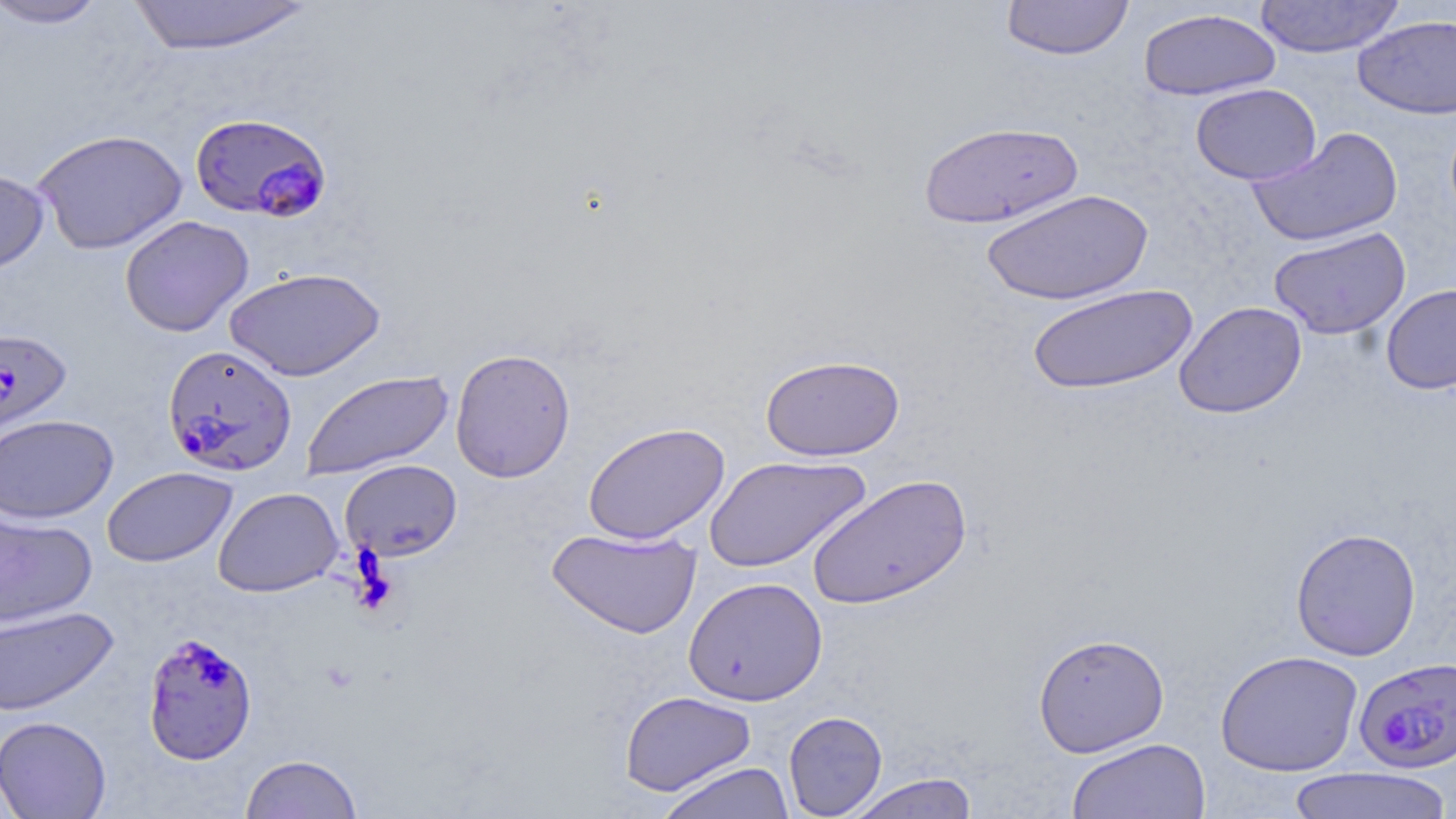

Approximate bounding boxes as (x1,y1)-(x2,y2) corner pairs in pixels. Plasmodium falciparum-infected red blood cell locations: (189,112)-(332,222), (0,328)-(72,443), (163,344)-(297,477), (142,630)-(258,765), (1353,657)-(1456,775). Uninfected red blood cell locations: (1,0)-(111,29), (126,0)-(317,56), (1001,0)-(1134,61), (1254,0)-(1405,58), (1137,8)-(1281,101), (1353,15)-(1456,119), (1190,83)-(1321,185), (918,120)-(1083,229), (1247,126)-(1404,248), (32,128)-(188,254), (0,168)-(50,274), (981,189)-(1153,305), (119,215)-(254,337), (1268,227)-(1411,339), (224,266)-(386,381), (1027,283)-(1197,396), (1380,284)-(1456,394), (1174,301)-(1307,418), (450,348)-(576,483), (761,353)-(904,461), (301,369)-(454,481), (0,414)-(118,524), (583,422)-(730,546), (704,455)-(871,574), (339,459)-(462,562), (101,466)-(237,567), (806,472)-(972,610), (213,486)-(343,596), (0,510)-(97,628), (547,526)-(701,639), (1290,527)-(1421,661), (683,576)-(828,706), (0,605)-(119,716), (1033,632)-(1170,757), (1215,649)-(1364,776), (619,690)-(756,795), (783,711)-(887,818), (0,716)-(111,819), (1067,737)-(1211,819), (240,753)-(363,818), (657,761)-(795,819), (1285,766)-(1453,819), (845,773)-(980,819). Slide-level diagnosis: Plasmodium falciparum. Optical microscopy. Single field of view. Image is 1456×819 pixels. Captured at 1000x magnification. May-Grünwald-Giemsa stain. Thin blood film.